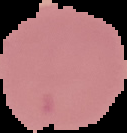
Image is 127×133 pixels. Malaria status: uninfected. The area outside the segmented cell region is set to black. From a thin blood film.